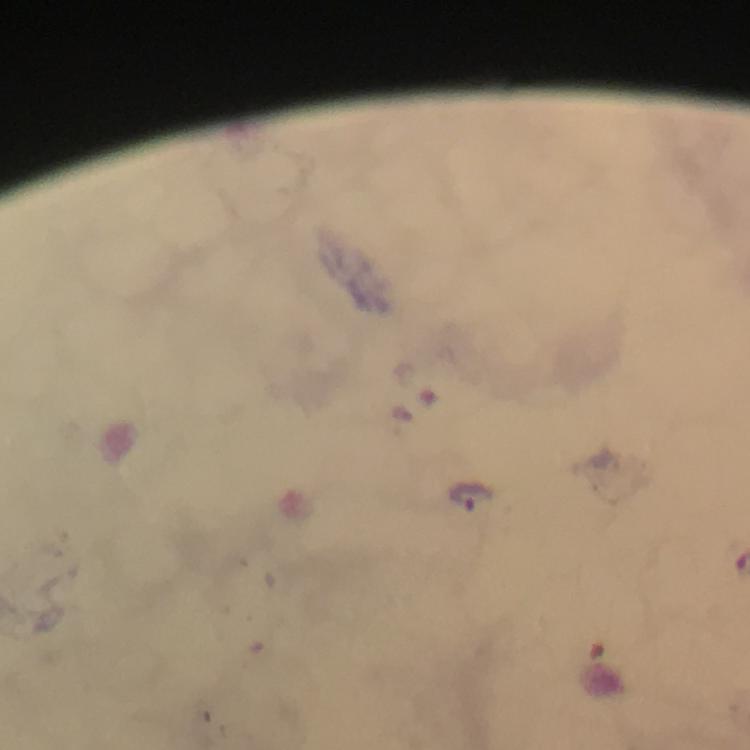

immersion oil = applied
preparation = thick blood film
cropped from = a single field of view
capture = smartphone photograph through a microscope
magnification = 100x
stain = Giemsa
image size = 750×750 pixels
malaria parasite locations = approximate centers as {x, y} in pixels: {405, 415}, {472, 497}
context = from a malaria diagnostic workup